Locate every Plasmodium ovale-infected red blood cell.
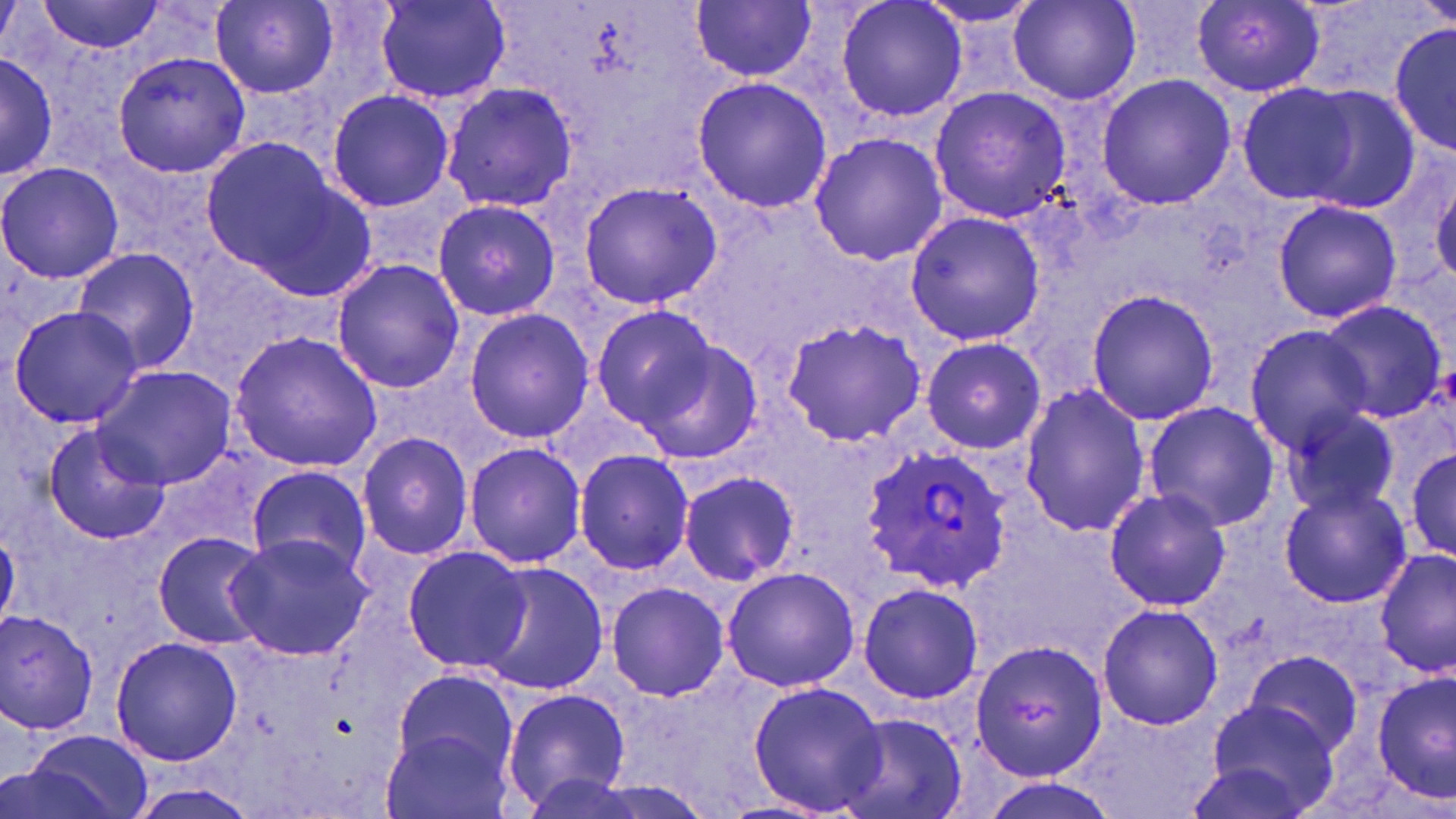

Approximate bounding boxes as (x1,y1)-(x2,y2) corner pairs in pixels.
Plasmodium ovale-infected red blood cells: (861,441)-(1015,591).

slide_level_diagnosis: Plasmodium ovale
image_size: 1456×819 pixels
field_of_view: one of a larger specimen
preparation: thin blood film
stain: May-Grünwald-Giemsa
modality: light microscopy
magnification: 1000x
uninfected_red_blood_cell_locations: 'approximate bounding boxes as (x1,y1)-(x2,y2) corner pairs in pixels: (375,0)-(511,106), (835,0)-(967,124), (38,1)-(166,52), (211,1)-(340,97), (691,1)-(816,84), (909,1)-(1048,31), (1008,1)-(1139,105), (1192,1)-(1326,94), (1388,18)-(1455,160), (0,48)-(61,182), (111,49)-(253,178), (1096,74)-(1237,210), (691,75)-(835,213), (1234,81)-(1361,204), (439,82)-(578,212), (1297,84)-(1426,214), (927,86)-(1072,221), (325,88)-(454,210), (809,131)-(950,267), (203,135)-(377,301), (0,161)-(125,284), (577,178)-(723,311), (1430,178)-(1456,285), (431,197)-(561,320), (1271,198)-(1402,323), (905,207)-(1044,348), (72,248)-(200,374), (330,258)-(466,394), (1083,286)-(1221,427), (1311,299)-(1448,423), (592,303)-(720,431), (8,305)-(146,428), (463,308)-(594,443), (778,320)-(926,445), (1245,325)-(1375,451), (228,331)-(383,471), (625,334)-(765,467), (921,336)-(1046,455), (93,366)-(234,491), (1019,381)-(1150,537), (1142,400)-(1281,532), (1280,405)-(1401,519), (37,420)-(170,546), (355,430)-(474,561), (463,441)-(587,568), (1405,441)-(1454,569), (573,449)-(695,575), (247,465)-(372,578), (679,471)-(801,586), (1279,484)-(1411,607), (1104,487)-(1232,611), (151,531)-(271,648), (223,533)-(375,662), (400,546)-(531,674), (1375,547)-(1455,678), (477,565)-(608,696), (721,565)-(860,692), (604,580)-(731,702), (856,581)-(983,704), (1097,602)-(1223,731), (2,612)-(101,733), (110,634)-(242,767), (971,640)-(1106,781), (1241,651)-(1366,763), (394,667)-(517,777), (1373,672)-(1454,802), (746,677)-(888,817), (502,688)-(633,811), (1197,698)-(1341,819), (836,710)-(967,819), (19,727)-(153,819), (378,728)-(514,819), (127,786)-(260,818)'